Assess this cell for malaria.
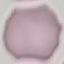
It is uninfected.

Summary:
  - Stain: Giemsa
  - Preparation: thin blood smear
  - Capture: smartphone camera at the microscope eyepiece
  - Image type: cell patch, automatically extracted from a larger field of view and resized to 64 × 64 pixels